Assess the morphology of the erythrocytes.
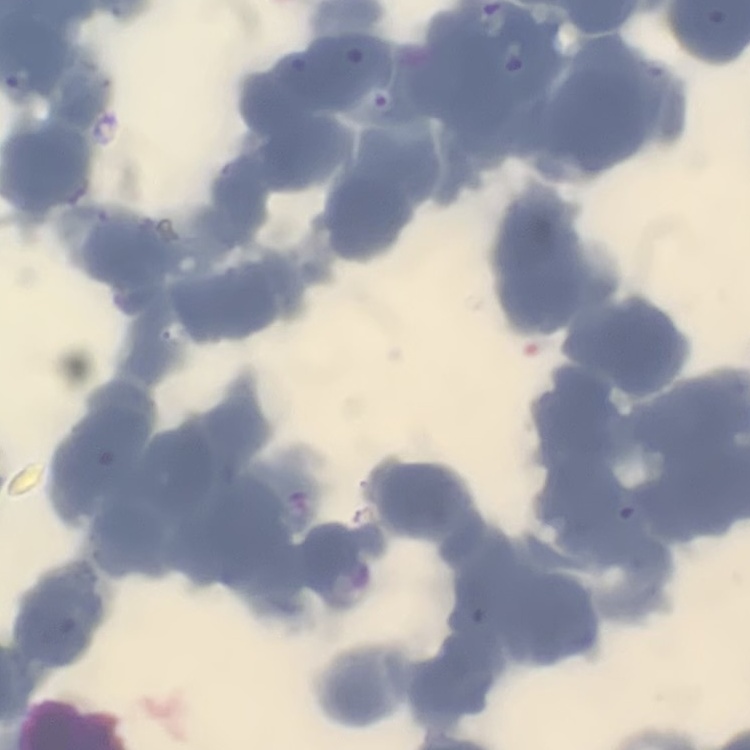
They show rouleaux formation.

Thin blood film. Stained with either Field's or Giemsa. One tile cut from a larger photomicrograph.